Comment on the morphology of the erythrocytes.
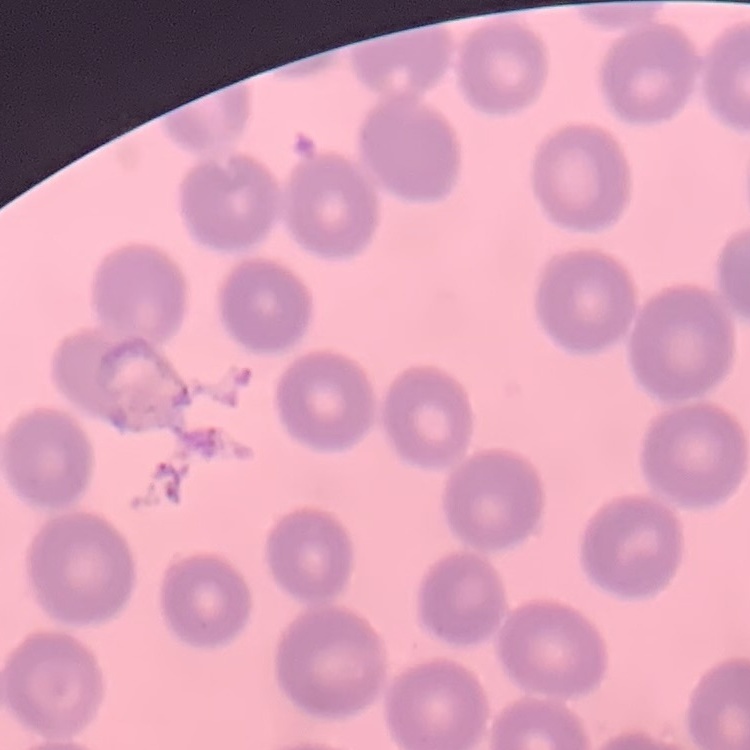

No rouleaux formation.

{
  "preparation": "thin blood smear",
  "image_type": "square crop of a larger photomicrograph",
  "stain": "Field's or Giemsa"
}